Assess this cell for malaria.
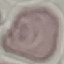

Uninfected.

Acquired by smartphone through the microscope eyepiece. Giemsa stain. Cell patch, automatically extracted from a larger field of view and resized to 64 × 64 pixels. Thin blood smear.